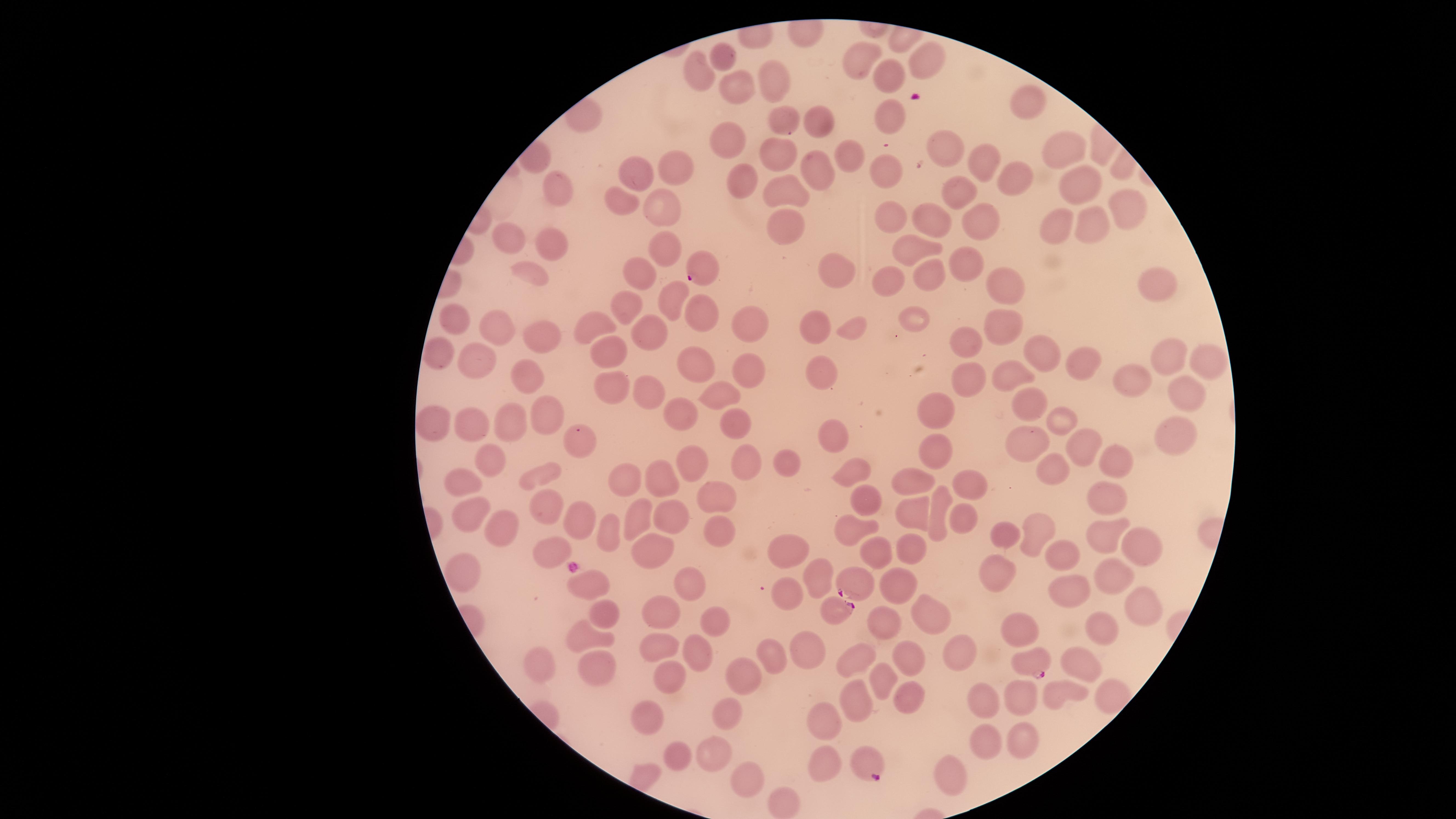

Approximate marker points as {x, y} in pixels. Uninfected red blood cells: {861, 55}, {723, 58}, {927, 59}, {694, 65}, {888, 78}, {774, 83}, {735, 84}, {1031, 101}, {894, 115}, {776, 117}, {820, 118}, {726, 143}, {942, 145}, {1062, 153}, {779, 156}, {848, 156}, {977, 163}, {674, 168}, {634, 170}, {818, 170}, {885, 170}, {1011, 179}, {738, 181}, {553, 186}, {783, 190}, {1074, 191}, {958, 196}, {618, 199}, {659, 207}, {1119, 210}, {929, 215}, {889, 217}, {975, 219}, {1096, 224}, {784, 225}, {1061, 228}, {508, 240}, {549, 243}, {667, 249}, {906, 250}, {963, 253}, {640, 270}, {534, 272}, {833, 272}, {924, 276}, {892, 283}, {1009, 283}, {1154, 284}, {667, 294}, {630, 311}, {697, 313}, {916, 316}, {450, 320}, {751, 324}, {998, 324}, {813, 326}, {594, 327}, {495, 328}, {855, 328}, {535, 330}, {649, 331}, {608, 349}, {978, 350}, {439, 354}, {1042, 356}, {1172, 360}, {694, 361}, {1076, 363}, {1201, 364}, {474, 365}, {740, 373}, {1008, 373}, {827, 374}, {531, 379}, {1123, 381}, {967, 382}, {616, 391}, {1190, 391}, {647, 394}, {716, 395}, {1022, 402}, {543, 411}, {934, 411}, {675, 412}, {512, 416}, {1062, 423}, {437, 424}, {738, 424}, {470, 426}, {1173, 428}, {831, 436}, {1018, 442}, {1082, 442}, {583, 443}, {938, 446}, {495, 458}, {1113, 462}, {691, 464}, {745, 464}, {788, 464}, {848, 468}, {1052, 468}, {544, 473}, {468, 475}, {620, 478}, {915, 478}, {661, 480}, {966, 483}, {720, 494}, {867, 495}, {1101, 495}, {546, 499}, {466, 508}, {911, 509}, {934, 512}, {636, 518}, {670, 518}, {573, 519}, {962, 519}, {717, 527}, {853, 528}, {610, 529}, {499, 530}, {1035, 532}, {1007, 533}, {1107, 537}, {1142, 545}, {783, 546}, {870, 547}, {911, 547}, {653, 550}, {552, 554}, {1067, 555}, {998, 568}, {1116, 573}, {583, 577}, {465, 579}, {819, 579}, {689, 581}, {898, 583}, {1069, 590}, {785, 592}, {1143, 603}, {658, 607}, {605, 611}, {930, 611}, {715, 618}, {883, 622}, {1017, 627}, {1101, 628}, {578, 632}, {660, 647}, {696, 647}, {804, 650}, {771, 655}, {957, 655}, {910, 657}, {854, 661}, {1077, 664}, {544, 665}, {599, 666}, {739, 668}, {878, 675}, {678, 679}, {1058, 691}, {1111, 691}, {905, 693}, {1016, 695}, {984, 700}, {851, 704}, {724, 709}, {645, 716}, {825, 724}, {988, 737}, {1017, 739}, {710, 754}, {679, 758}, {823, 758}, {742, 777}, {952, 781}, {783, 802}. Parasitized red blood cells: {699, 268}, {856, 584}, {836, 612}, {1029, 665}, {867, 761}. Presence: malaria parasites detected. Photographed with a smartphone camera through the microscope eyepiece. Giemsa-stained preparation. Single field of view. The visible region is circular. Species: Plasmodium falciparum. Image is 1456×819 pixels. Thin blood film.